Assess this cell for malaria.
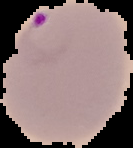
It is parasitized.

Summary:
  - Preparation: thin blood smear
  - Image size: 133×148 pixels
  - Image type: segmented cell region with the area outside set to black